State the blood parasite species.
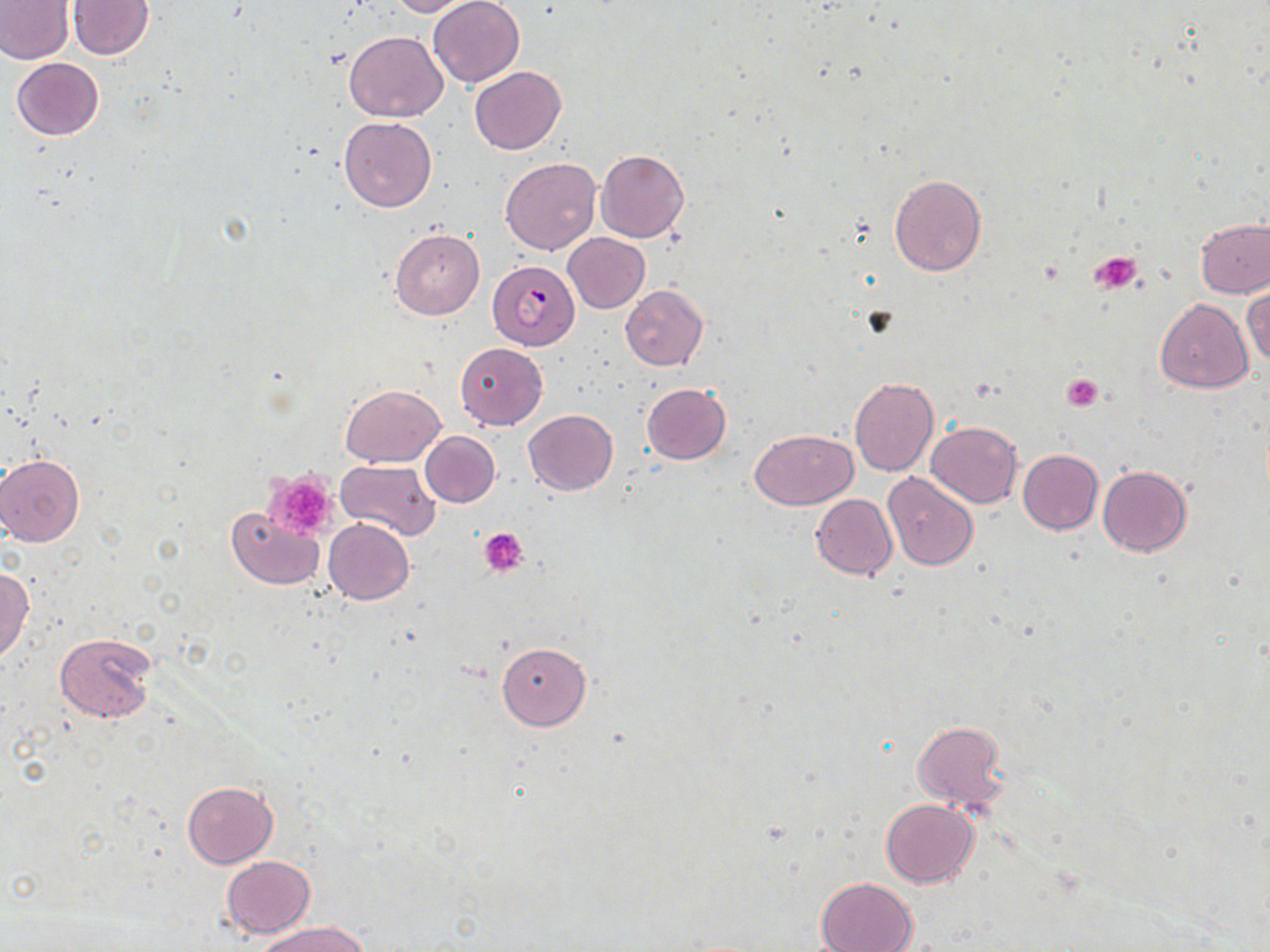

Plasmodium falciparum.

magnification = 1000x
uninfected red blood cell locations = approximate bounding boxes as named x1/y1/x2/y2 corners in pixels: (x1=0, y1=0, x2=73, y2=64), (x1=67, y1=0, x2=155, y2=59), (x1=386, y1=0, x2=480, y2=17), (x1=428, y1=0, x2=524, y2=87), (x1=343, y1=30, x2=448, y2=122), (x1=11, y1=58, x2=105, y2=141), (x1=469, y1=66, x2=566, y2=154), (x1=338, y1=115, x2=437, y2=213), (x1=597, y1=149, x2=689, y2=242), (x1=500, y1=157, x2=600, y2=255), (x1=889, y1=174, x2=986, y2=277), (x1=1195, y1=219, x2=1270, y2=298), (x1=390, y1=229, x2=485, y2=320), (x1=562, y1=233, x2=650, y2=313), (x1=1243, y1=284, x2=1270, y2=369), (x1=619, y1=285, x2=708, y2=371), (x1=1154, y1=299, x2=1253, y2=393), (x1=455, y1=342, x2=549, y2=429), (x1=849, y1=376, x2=938, y2=476), (x1=641, y1=383, x2=731, y2=464), (x1=339, y1=384, x2=446, y2=466), (x1=523, y1=409, x2=618, y2=495), (x1=926, y1=421, x2=1022, y2=509), (x1=750, y1=428, x2=857, y2=509), (x1=420, y1=432, x2=499, y2=508), (x1=1017, y1=448, x2=1102, y2=535), (x1=0, y1=454, x2=86, y2=547), (x1=336, y1=459, x2=440, y2=540), (x1=1097, y1=465, x2=1192, y2=557), (x1=883, y1=472, x2=977, y2=570), (x1=812, y1=494, x2=896, y2=580), (x1=226, y1=507, x2=323, y2=589), (x1=323, y1=518, x2=414, y2=605), (x1=0, y1=566, x2=34, y2=661), (x1=54, y1=630, x2=156, y2=724), (x1=496, y1=641, x2=591, y2=729), (x1=911, y1=720, x2=1009, y2=812), (x1=182, y1=780, x2=277, y2=867), (x1=881, y1=798, x2=978, y2=887), (x1=221, y1=855, x2=315, y2=937), (x1=814, y1=878, x2=919, y2=952), (x1=254, y1=920, x2=372, y2=951)
preparation = thin blood smear
platelet locations = approximate bounding boxes as named x1/y1/x2/y2 corners in pixels: (x1=1091, y1=252, x2=1142, y2=295), (x1=1061, y1=374, x2=1103, y2=411), (x1=264, y1=472, x2=337, y2=541), (x1=481, y1=527, x2=529, y2=576)
modality = light microscopy
stain = May-Grünwald-Giemsa
image size = 1270×952 pixels
Plasmodium falciparum-infected red blood cell locations = approximate bounding boxes as named x1/y1/x2/y2 corners in pixels: (x1=487, y1=260, x2=580, y2=350)
field of view = single